Classify this cell by malaria status.
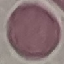

It is uninfected.

Summary:
  - Preparation: thin blood smear
  - Stain: Giemsa
  - Image type: cell patch, automatically extracted from a larger field of view and resized to 64 × 64 pixels
  - Capture: smartphone through the microscope eyepiece